State which parasite is depicted.
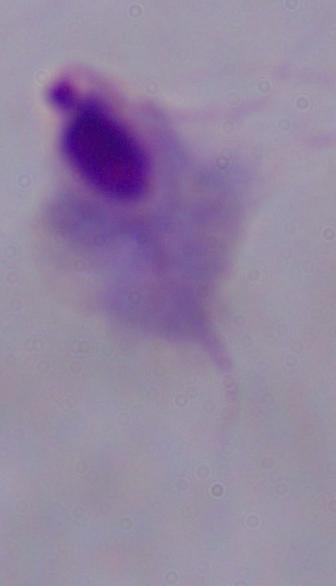
This is a trichomonad.

modality = micrograph
magnification = 1000x